Locate every Plasmodium vivax-infected red blood cell.
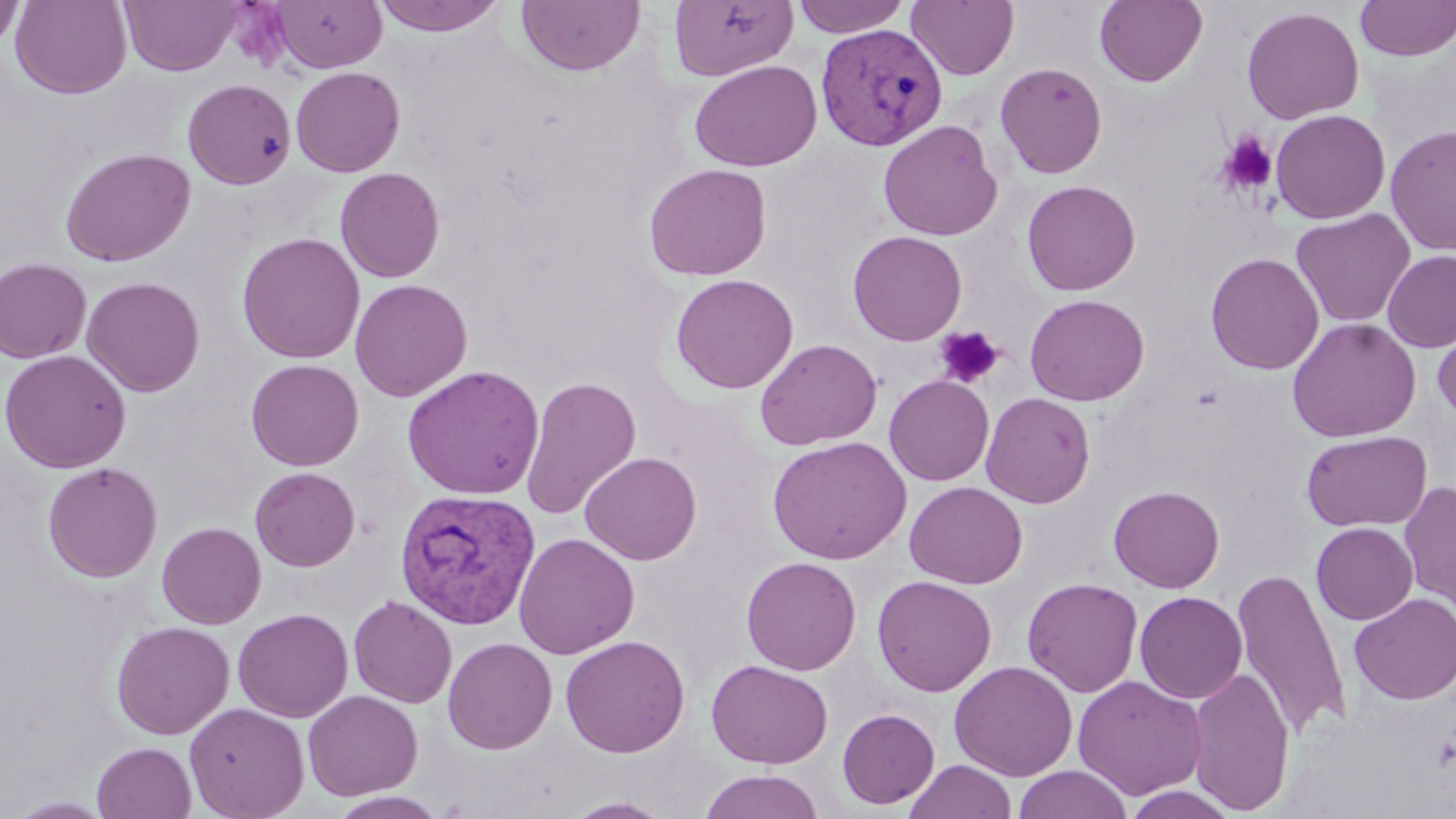
Approximate bounding boxes as (x1, y1, x2, y2) in pixels.
Plasmodium vivax-infected red blood cells: (815, 23, 948, 151), (394, 487, 541, 630).

Summary:
  - Platelet locations: (1216, 131, 1278, 196), (934, 325, 1003, 388)
  - Uninfected red blood cell locations: (11, 0, 131, 98), (120, 0, 240, 75), (271, 0, 387, 73), (370, 0, 508, 37), (669, 0, 798, 81), (792, 0, 911, 38), (1094, 0, 1208, 87), (0, 1, 23, 50), (517, 1, 645, 76), (907, 1, 1019, 80), (1355, 1, 1456, 62), (1241, 6, 1365, 124), (690, 59, 821, 172), (995, 61, 1108, 179), (291, 66, 406, 177), (183, 78, 296, 189), (1270, 109, 1391, 224), (878, 119, 1003, 241), (1385, 124, 1456, 256), (59, 146, 196, 267), (643, 163, 771, 281), (335, 167, 445, 282), (1021, 179, 1141, 296), (1290, 208, 1416, 327), (847, 230, 967, 344), (237, 232, 365, 364), (1382, 250, 1456, 352), (1205, 252, 1324, 374), (0, 258, 92, 363), (670, 273, 798, 394), (82, 276, 205, 397), (350, 278, 472, 401), (1024, 293, 1150, 406), (1434, 308, 1456, 425), (1287, 317, 1422, 442), (755, 338, 882, 451), (0, 349, 132, 472), (245, 358, 364, 470), (402, 365, 544, 500), (520, 375, 641, 520), (884, 375, 994, 486), (980, 392, 1096, 508), (1301, 430, 1432, 532), (768, 436, 911, 564), (580, 451, 702, 565), (42, 461, 162, 582), (250, 466, 360, 571), (904, 481, 1028, 588), (1398, 481, 1456, 614), (1109, 484, 1225, 593), (157, 521, 267, 629), (1311, 523, 1418, 624), (514, 532, 640, 659), (741, 556, 861, 675), (1232, 568, 1351, 739), (872, 575, 997, 697), (1022, 577, 1144, 698), (1134, 591, 1248, 703), (1350, 593, 1456, 704), (349, 595, 457, 708), (233, 608, 353, 723), (111, 620, 235, 739), (560, 635, 690, 757), (442, 637, 558, 754), (706, 658, 833, 768), (949, 660, 1078, 781), (1187, 667, 1296, 814), (1073, 676, 1207, 799), (303, 690, 423, 800), (185, 702, 310, 819), (837, 708, 940, 809), (92, 741, 196, 819), (904, 759, 1017, 819), (1013, 765, 1133, 819), (698, 769, 825, 819), (1120, 785, 1243, 819), (328, 791, 450, 819), (7, 796, 116, 818), (561, 796, 675, 818)
  - Slide-level diagnosis: Plasmodium vivax
  - Preparation: thin blood smear
  - Stain: May-Grünwald-Giemsa
  - Magnification: 1000x
  - Modality: optical microscopy
  - Field of view: one of a larger specimen
  - Image size: 1456×819 pixels